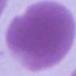
modality = micrograph
identification = erythrocyte
magnification = 1000x